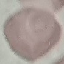
Result: no malaria parasites detected. Photographed with a smartphone camera at the microscope eyepiece. Giemsa stain. Thin smear of blood. Automatically extracted cell patch, resized to 64 × 64 pixels.